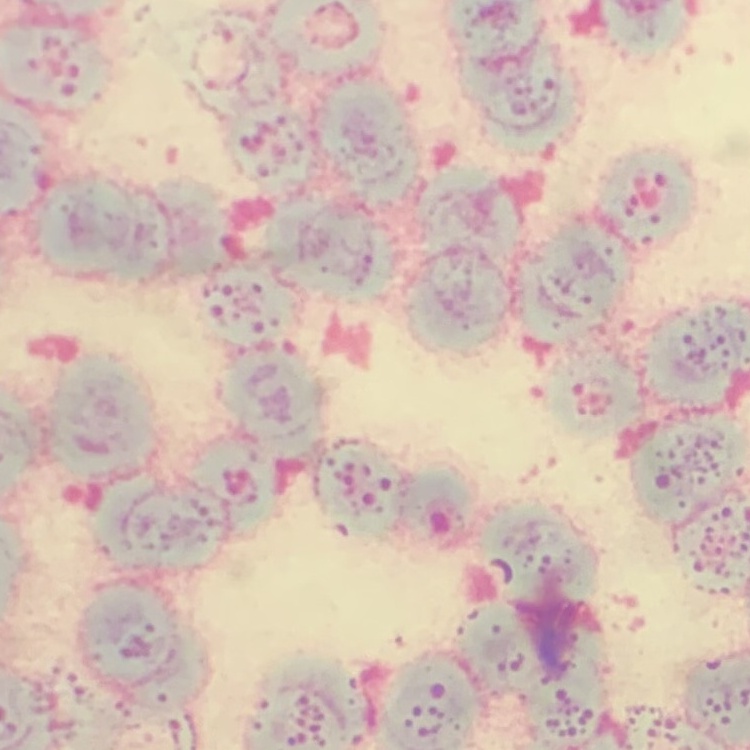

The red blood cells exhibit rouleaux formation. Thin blood film. One tile cut from a larger photomicrograph. Field's or Giemsa stain.